State which parasite is depicted.
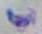

Toxoplasma gondii.

modality = micrograph
magnification = 1000x